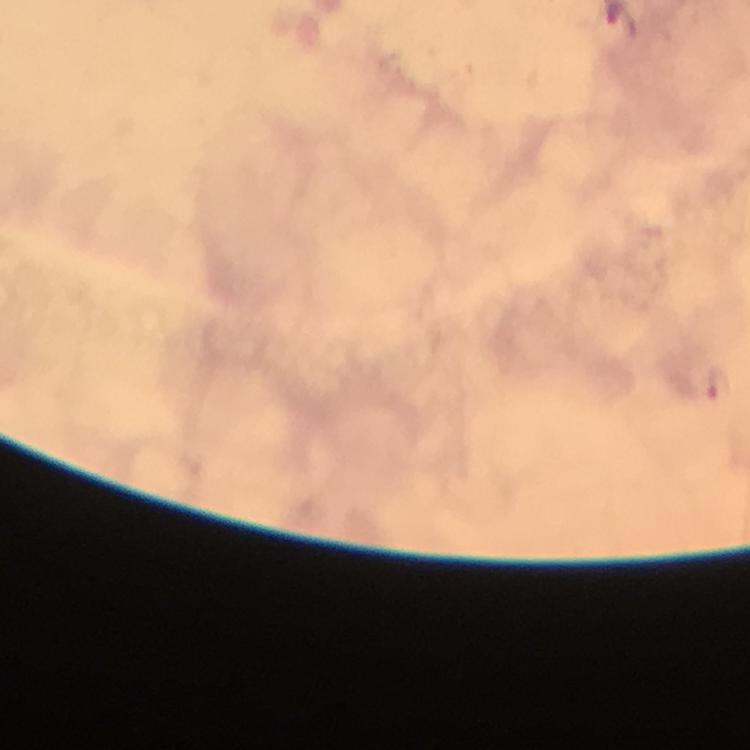

Approximate centers as (x, y) in pixels.
Summary:
  - Plasmodium parasite locations: (719, 382)
  - Stain: Giemsa
  - Magnification: 100x
  - Immersion oil: used
  - Image size: 750×750 pixels
  - Capture: smartphone camera through the microscope
  - Context: from a diagnostic examination for malaria
  - Cropped from: one field of view
  - Preparation: thick blood smear